Assess the morphology of the red blood cells.
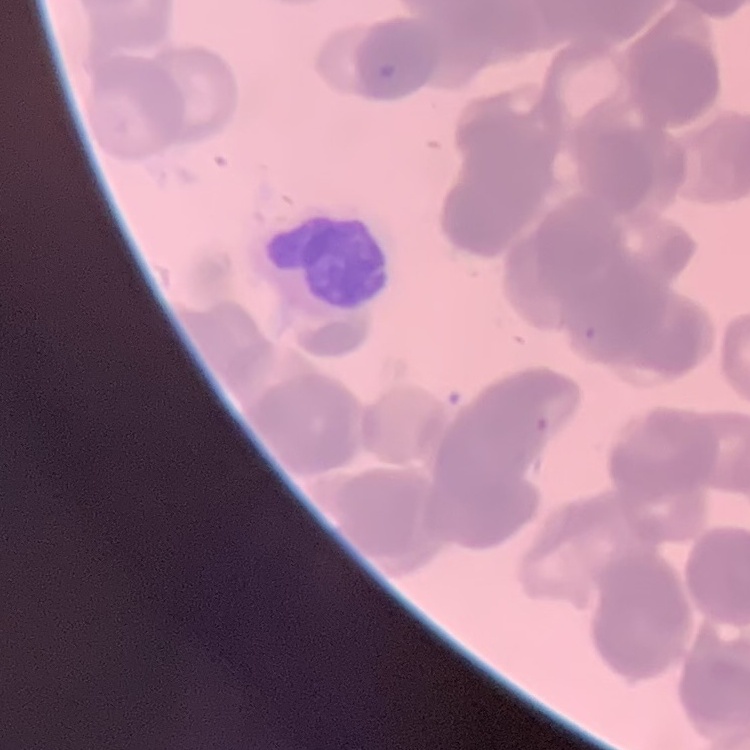

Rouleaux formation.

preparation: thin blood film
image_type: one tile cut from a larger photomicrograph
stain: Field's or Giemsa